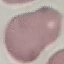
Malaria status: uninfected. Giemsa stain. Cell patch, automatically extracted from a larger field of view and resized to 64 × 64 pixels. Thin smear of blood. Acquired by smartphone through the microscope eyepiece.